Locate every Plasmodium parasite.
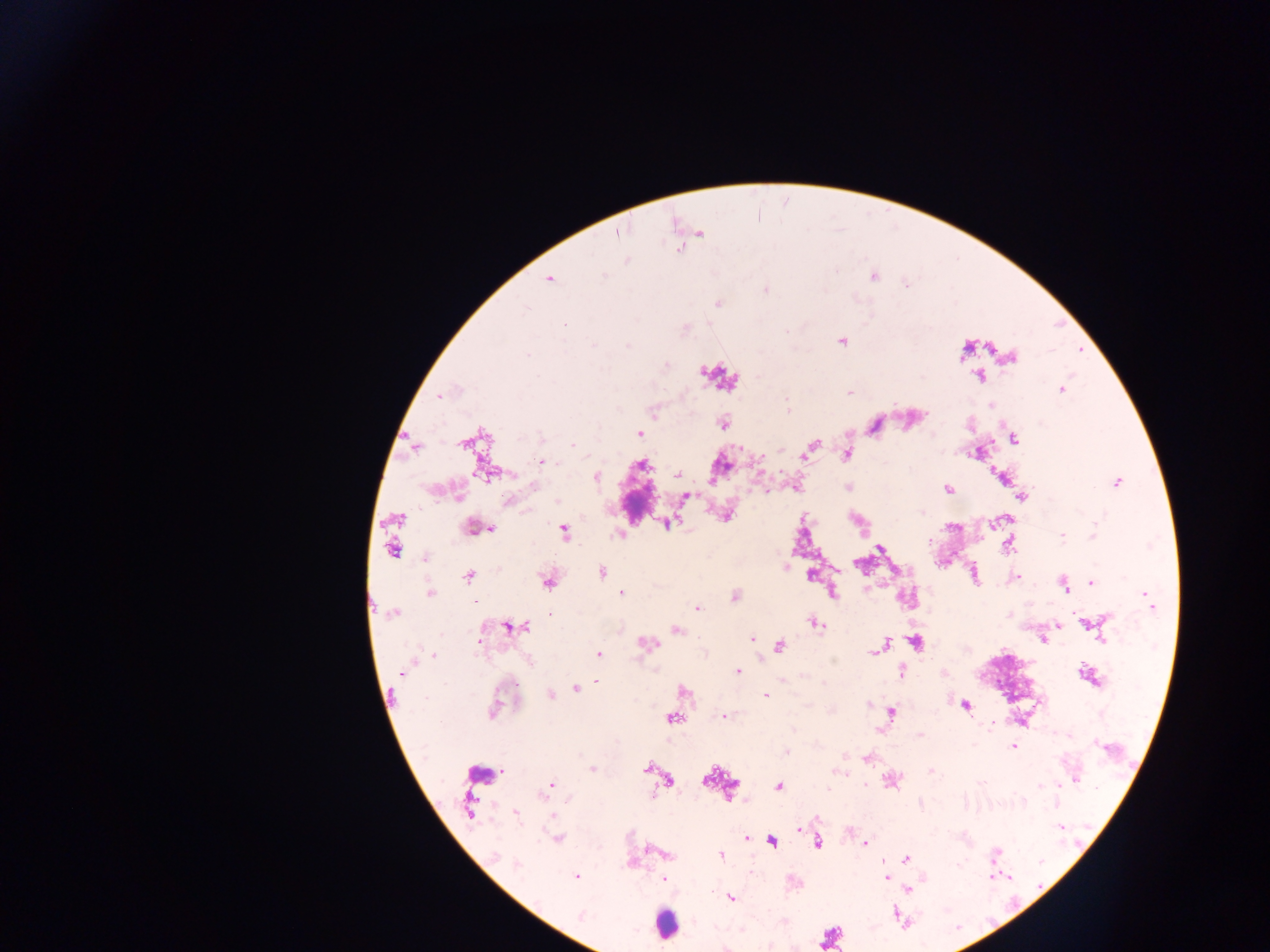
Approximate centers as [x, y] in pixels.
Plasmodium parasites: [615, 234], [700, 234], [679, 249], [627, 261], [602, 276], [875, 277], [547, 280], [766, 289], [524, 307], [787, 331], [1060, 391], [438, 395], [787, 409], [639, 433], [573, 444], [461, 446], [541, 462], [596, 476], [1118, 482], [765, 490], [726, 516], [1061, 538], [424, 558], [497, 568], [602, 573], [1017, 576], [1091, 583], [1066, 590], [622, 592], [430, 593], [1144, 595], [474, 600], [697, 606], [1153, 608], [393, 613], [1074, 613], [551, 615], [1058, 625], [677, 629], [751, 639], [480, 640], [433, 655], [599, 656], [530, 662], [900, 672], [944, 672], [400, 673], [737, 673], [598, 679], [518, 686], [765, 694], [724, 718], [988, 727], [1012, 747], [788, 752], [646, 767], [845, 774], [1075, 779], [551, 782], [779, 787], [568, 799], [515, 814], [551, 815], [1057, 826], [799, 831], [558, 838], [747, 838], [817, 844], [865, 844], [995, 851], [721, 853], [668, 854], [906, 860], [516, 864], [635, 864], [576, 878], [662, 878], [885, 878], [908, 889], [732, 898], [894, 911].

{
  "leukocyte_locations": "approximate centers as [x, y] in pixels: [665, 927]",
  "country": "Ghana",
  "preparation": "thick blood film",
  "image_size": "1270×952 pixels",
  "capture": "mobile-phone photograph through a microscope",
  "field_of_view": "single"
}